Give the position of every Plasmodium parasite visible.
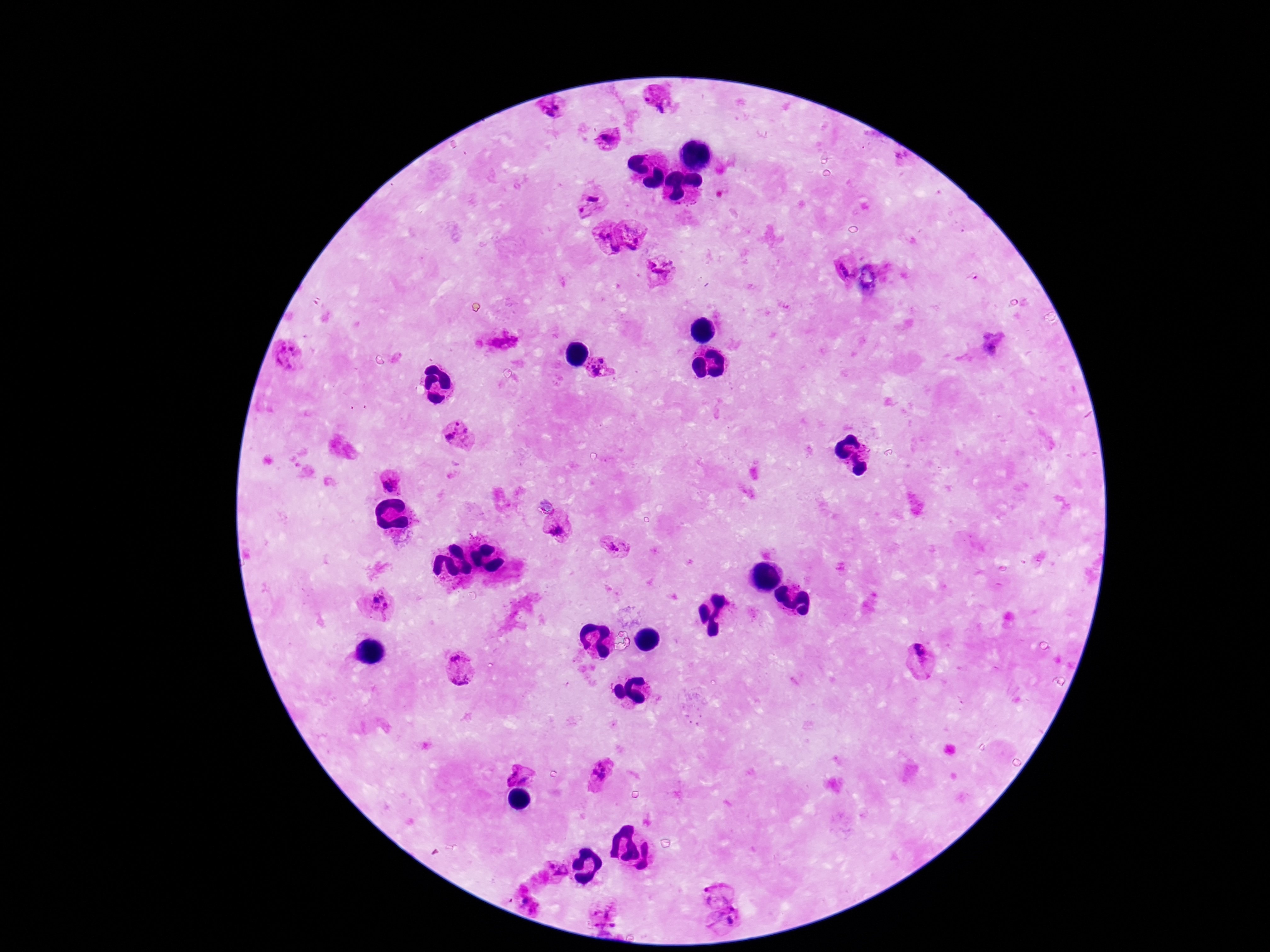
Approximate centers as (x, y) in pixels.
Plasmodium parasites: (659, 101), (552, 108), (607, 137), (594, 196), (581, 210), (604, 232), (635, 235), (616, 248), (660, 268), (845, 271), (974, 278), (992, 346), (289, 355), (601, 368), (459, 435), (389, 483), (559, 532), (615, 547), (380, 603), (456, 656), (919, 657), (463, 682), (520, 774), (603, 774), (555, 870), (717, 892), (604, 915), (729, 921).

stain = Giemsa
patient malaria status = infected
capture = smartphone camera through the microscope eyepiece
preparation = thick peripheral-blood smear
magnification = 100x
field of view = one from this slide
image size = 1270×952 pixels